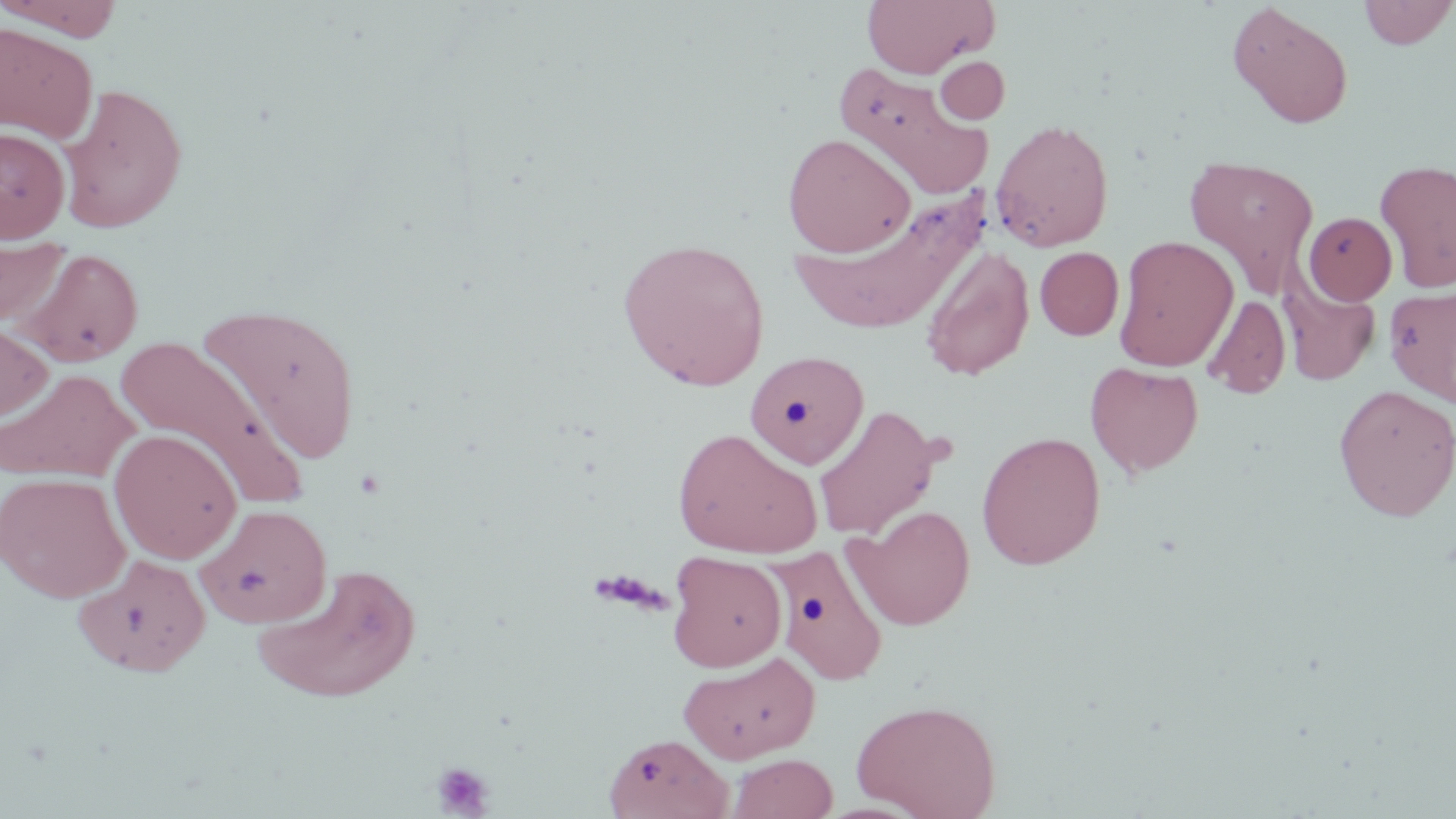

Summary:
  - Coordinate format: approximate bounding boxes as (x1, y1, x2, y2) in pixels
  - Platelet locations: (432, 761, 495, 817)
  - Uninfected red blood cell locations: (1, 0, 124, 40), (862, 0, 995, 77), (1358, 0, 1455, 48), (1227, 3, 1354, 129), (0, 22, 98, 144), (935, 56, 1010, 124), (834, 62, 992, 197), (58, 83, 188, 233), (990, 118, 1115, 252), (0, 127, 70, 243), (782, 132, 916, 257), (1184, 154, 1320, 296), (1375, 159, 1456, 292), (788, 194, 987, 337), (1303, 211, 1397, 305), (0, 233, 71, 328), (1114, 235, 1239, 372), (618, 239, 770, 390), (1037, 242, 1217, 349), (16, 247, 144, 367), (1035, 247, 1124, 340), (919, 248, 1034, 381), (1279, 271, 1381, 386), (1383, 286, 1456, 405), (1203, 294, 1291, 399), (198, 301, 363, 464), (0, 319, 52, 426), (114, 334, 309, 509), (745, 349, 870, 469), (1085, 361, 1203, 477), (0, 368, 138, 482), (1334, 384, 1456, 520), (812, 405, 946, 541), (672, 428, 823, 557), (109, 429, 242, 564), (976, 430, 1106, 569), (1, 471, 131, 603), (196, 503, 332, 629), (848, 505, 975, 630), (771, 544, 889, 685), (668, 551, 786, 671), (72, 553, 212, 677), (253, 563, 422, 704), (678, 651, 821, 763), (851, 698, 1001, 819), (603, 733, 733, 818), (727, 753, 838, 819)
  - Slide-level diagnosis: negative for blood parasites
  - Modality: optical microscopy
  - Field of view: one of a larger specimen
  - Magnification: 1000x
  - Preparation: thin blood smear
  - Image size: 1456×819 pixels
  - Stain: May-Grünwald-Giemsa